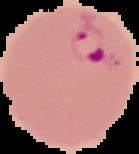

Summary:
  - Image type: segmented cell region with the area outside set to black
  - Result: Plasmodium parasites detected
  - Preparation: thin blood smear
  - Image size: 139×154 pixels